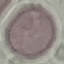

Summary:
  - Result: no malaria parasites detected
  - Image type: cell patch, automatically extracted from a larger field of view and resized to 64 × 64 pixels
  - Capture: smartphone camera at the microscope eyepiece
  - Stain: Giemsa
  - Preparation: thin blood film